Outline each Babesia divergens-infected red blood cell.
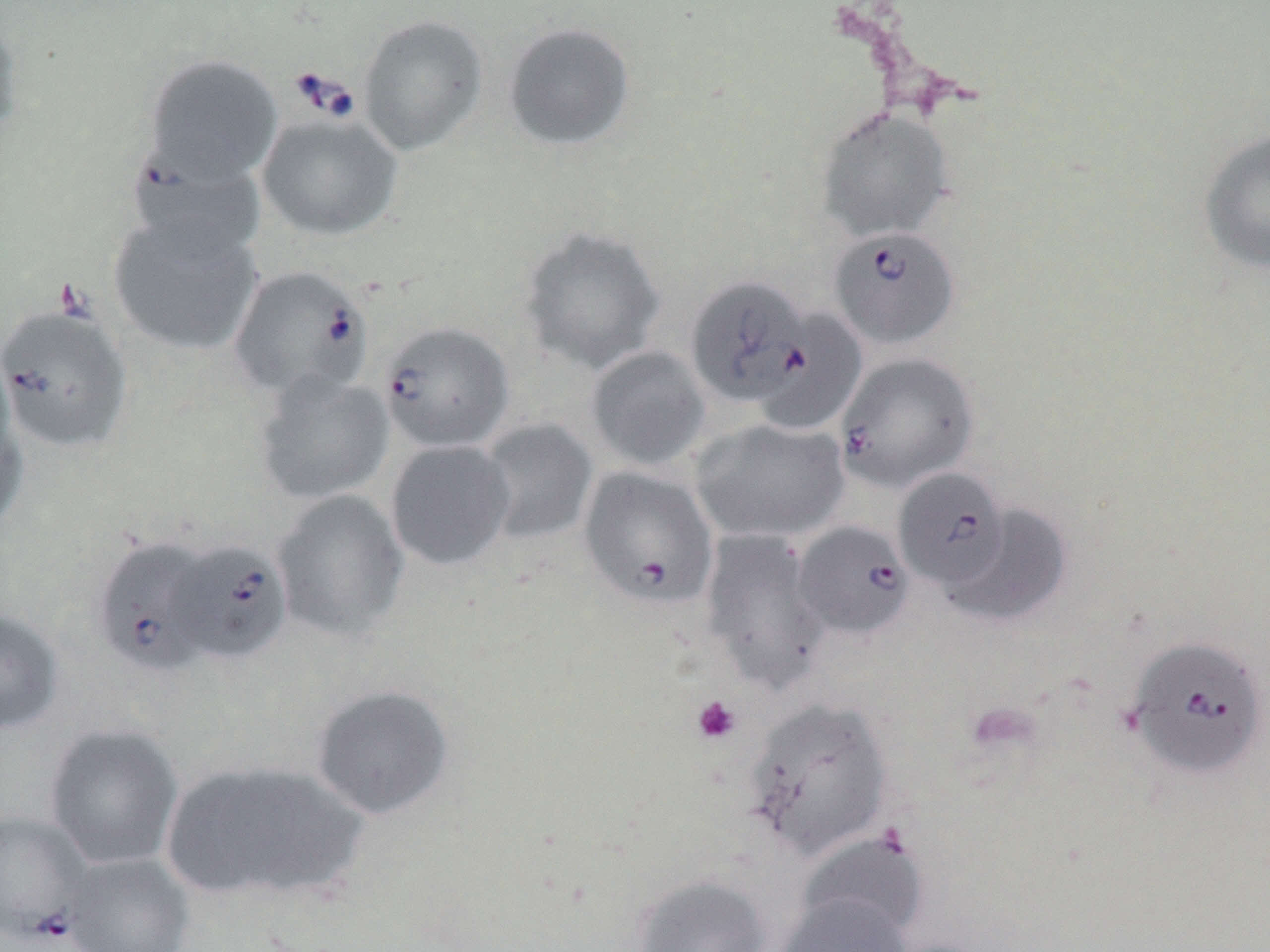

Approximate bounding boxes as named x1/y1/x2/y2 corners in pixels.
Babesia divergens-infected red blood cells: (x1=126, y1=150, x2=265, y2=263), (x1=828, y1=226, x2=960, y2=350), (x1=228, y1=265, x2=372, y2=402), (x1=686, y1=276, x2=813, y2=407), (x1=0, y1=303, x2=135, y2=453), (x1=378, y1=321, x2=515, y2=453), (x1=834, y1=351, x2=979, y2=493), (x1=578, y1=466, x2=718, y2=610), (x1=893, y1=467, x2=1013, y2=592), (x1=793, y1=520, x2=914, y2=639), (x1=92, y1=537, x2=216, y2=678), (x1=171, y1=539, x2=292, y2=665), (x1=1124, y1=634, x2=1270, y2=780), (x1=0, y1=810, x2=91, y2=942).

Platelet locations: (x1=690, y1=695, x2=742, y2=744). Uninfected red blood cell locations: (x1=0, y1=10, x2=26, y2=147), (x1=358, y1=14, x2=489, y2=156), (x1=502, y1=22, x2=636, y2=152), (x1=143, y1=54, x2=283, y2=184), (x1=816, y1=107, x2=954, y2=242), (x1=256, y1=113, x2=403, y2=241), (x1=1199, y1=130, x2=1270, y2=274), (x1=108, y1=211, x2=264, y2=357), (x1=518, y1=226, x2=666, y2=374), (x1=752, y1=307, x2=866, y2=436), (x1=586, y1=346, x2=711, y2=470), (x1=254, y1=371, x2=395, y2=505), (x1=0, y1=396, x2=29, y2=535), (x1=478, y1=418, x2=598, y2=545), (x1=690, y1=418, x2=850, y2=543), (x1=386, y1=440, x2=515, y2=571), (x1=272, y1=490, x2=409, y2=641), (x1=941, y1=502, x2=1072, y2=627), (x1=697, y1=528, x2=832, y2=695), (x1=0, y1=608, x2=66, y2=735), (x1=310, y1=684, x2=455, y2=820), (x1=743, y1=696, x2=895, y2=860), (x1=45, y1=724, x2=184, y2=870), (x1=159, y1=760, x2=370, y2=906), (x1=797, y1=832, x2=929, y2=942), (x1=63, y1=852, x2=195, y2=952), (x1=630, y1=873, x2=772, y2=952), (x1=775, y1=892, x2=912, y2=952). Slide-level diagnosis: Babesia divergens. 1000x magnification. Image is 1270×952 pixels. Thin blood smear. One field of a larger specimen. Optical microscopy. May-Grünwald-Giemsa stain.